Assess the morphology of the red blood cells.
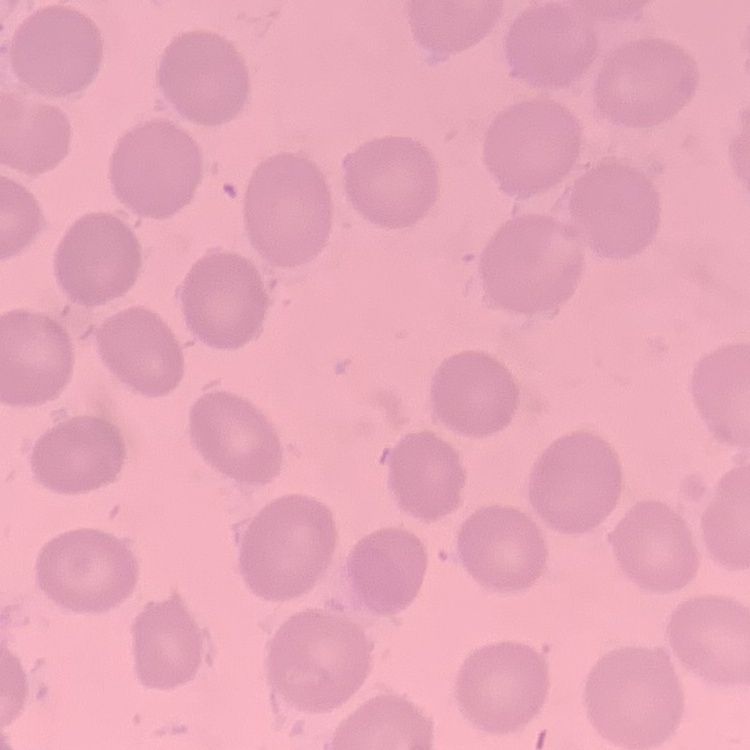

No rouleaux formation.

Summary:
  - Stain: Field's or Giemsa
  - Preparation: thin blood smear
  - Image type: square crop of a larger photomicrograph